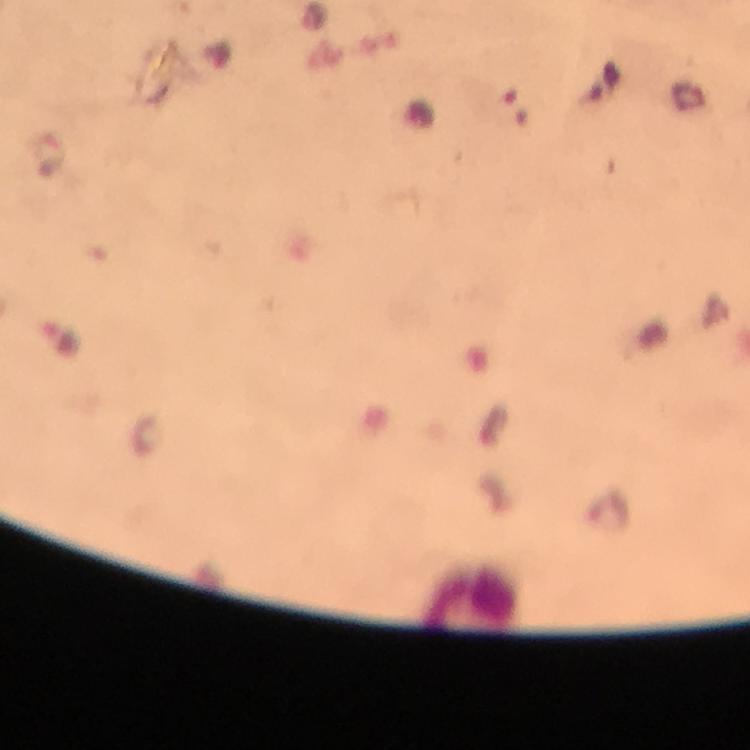

Approximate centers as [x, y] in pixels.
Summary:
  - Malaria parasite locations: [51, 153], [61, 338]
  - Context: from a diagnostic examination for malaria
  - Stain: Giemsa
  - Immersion oil: used
  - Cropped from: one field of view
  - Image size: 750×750 pixels
  - Magnification: 100x
  - Preparation: thick blood smear
  - Capture: smartphone photograph through a microscope